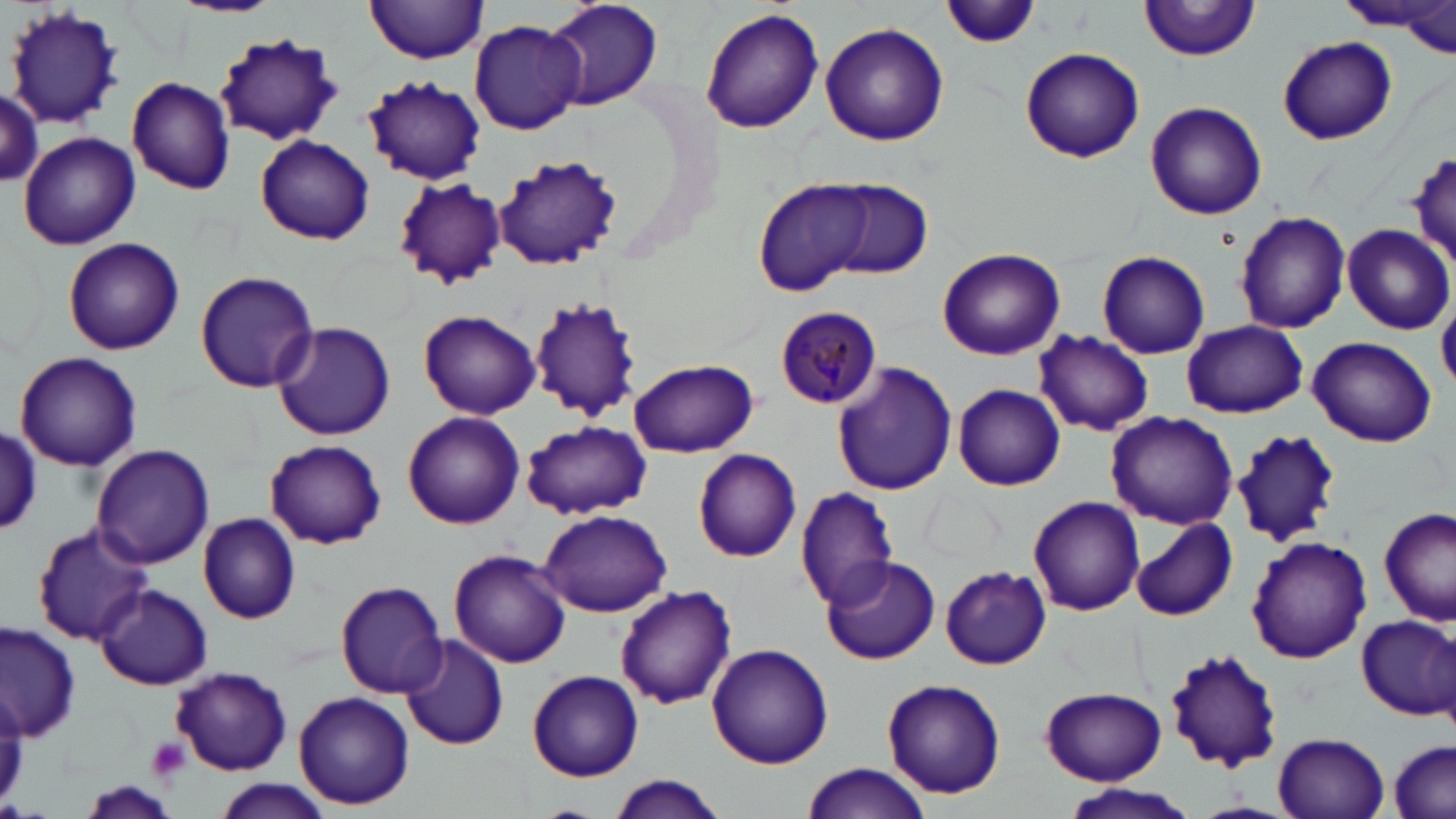
Approximate bounding boxes as [x1, y1, x2, y2] in pixels. Uninfected red blood cell locations: [173, 0, 283, 18], [365, 0, 489, 64], [544, 0, 664, 111], [940, 0, 1039, 50], [1139, 0, 1262, 61], [1343, 0, 1442, 35], [4, 3, 125, 130], [698, 8, 825, 136], [469, 19, 585, 134], [819, 22, 949, 146], [215, 34, 343, 145], [1279, 36, 1398, 146], [1020, 46, 1145, 163], [127, 75, 236, 194], [363, 75, 486, 185], [0, 87, 44, 186], [1145, 100, 1268, 220], [19, 132, 141, 250], [255, 136, 375, 247], [1408, 152, 1456, 264], [493, 156, 625, 270], [392, 176, 508, 288], [754, 178, 874, 297], [826, 180, 932, 278], [1234, 210, 1351, 333], [1341, 222, 1454, 333], [62, 237, 185, 356], [937, 247, 1065, 360], [1097, 250, 1210, 359], [194, 270, 320, 394], [528, 299, 644, 421], [418, 309, 540, 419], [1181, 319, 1307, 419], [271, 321, 397, 440], [1032, 331, 1154, 437], [1309, 336, 1437, 447], [15, 353, 143, 470], [627, 360, 759, 458], [831, 361, 957, 497], [953, 383, 1064, 490], [403, 411, 524, 529], [1106, 411, 1239, 530], [521, 420, 651, 520], [1, 429, 42, 533], [1230, 429, 1346, 548], [264, 439, 388, 549], [90, 444, 215, 571], [694, 449, 802, 561], [795, 485, 901, 609], [1027, 496, 1144, 617], [1378, 506, 1454, 626], [540, 507, 672, 617], [198, 512, 300, 623], [1132, 516, 1237, 622], [32, 524, 153, 644], [1246, 536, 1370, 663], [449, 550, 571, 668], [821, 555, 940, 665], [940, 566, 1051, 669], [335, 579, 445, 697], [94, 585, 212, 690], [615, 585, 736, 708], [1355, 613, 1456, 721], [1, 620, 80, 743], [397, 634, 508, 750], [706, 643, 834, 769], [1164, 650, 1284, 773], [171, 667, 293, 774], [528, 670, 644, 781], [880, 678, 1009, 799], [1039, 687, 1168, 787], [295, 690, 414, 811], [1273, 732, 1389, 818], [1388, 740, 1454, 818], [800, 762, 931, 819], [607, 775, 726, 819], [207, 779, 334, 819], [1063, 782, 1198, 819]. Plasmodium malariae-infected red blood cell locations: [773, 307, 884, 409]. Platelet locations: [145, 736, 190, 783]. Slide-level diagnosis: Plasmodium malariae. Thin blood film. One field of a larger specimen. 1000x magnification. May-Grünwald-Giemsa-stained preparation. Optical microscopy. Image is 1456×819 pixels.